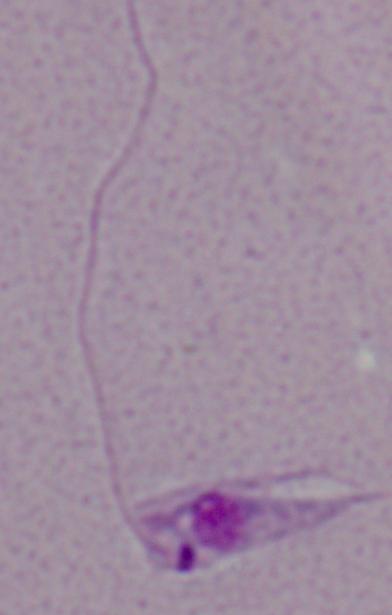

Summary:
  - Identification: Leishmania
  - Magnification: 1000x
  - Modality: photomicrograph